Give the extent of all Plasmodium malariae-infected red blood cells.
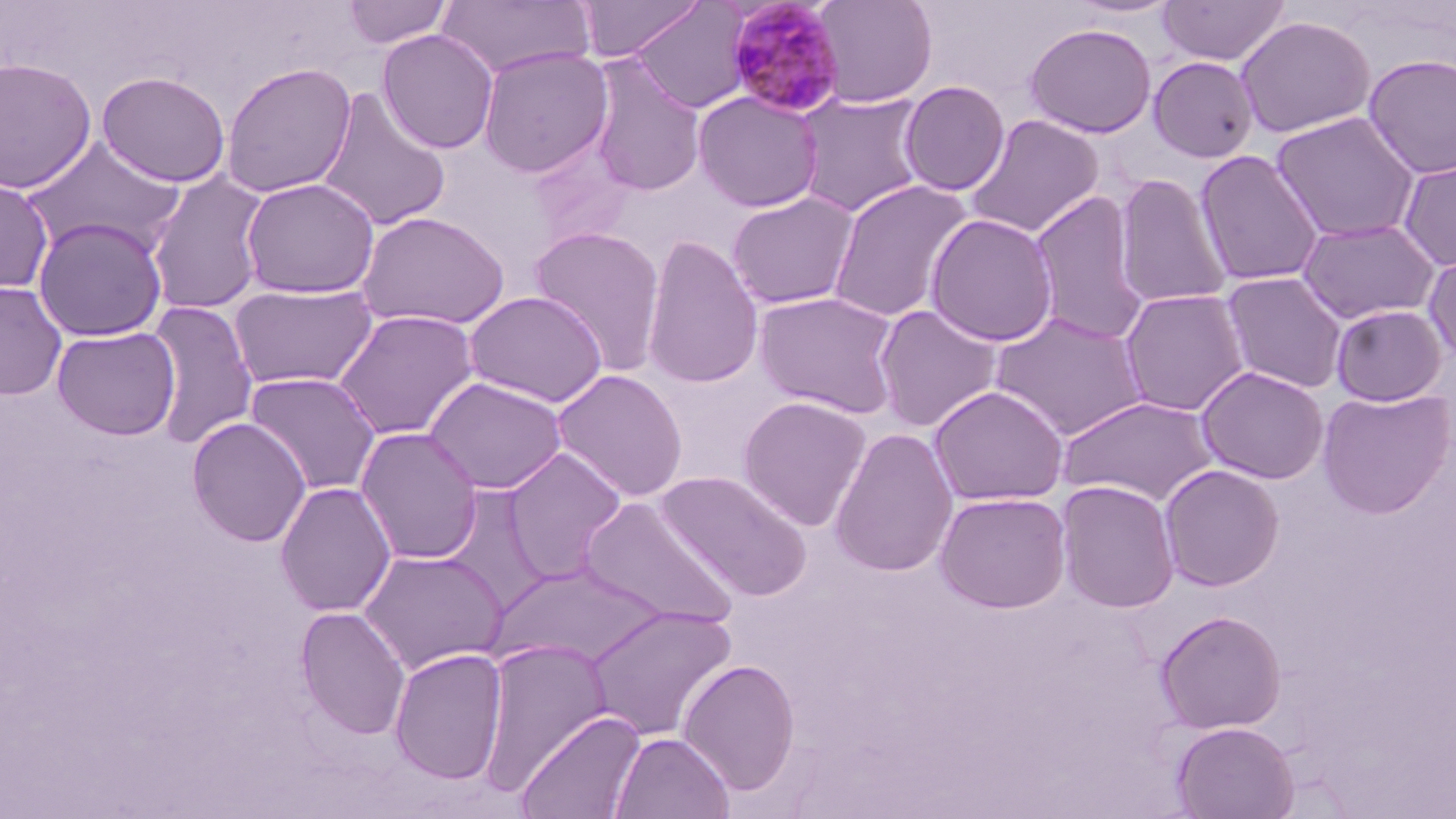

Approximate bounding boxes as (x1,y1)-(x2,y2) corner pairs in pixels.
Plasmodium malariae-infected red blood cells: (725,0)-(847,118).

slide-level diagnosis = Plasmodium malariae
field of view = one of a larger specimen
uninfected red blood cell locations = approximate bounding boxes as (x1,y1)-(x2,y2) corner pairs in pixels: (341,0)-(453,49), (573,0)-(704,62), (813,0)-(938,107), (1064,0)-(1182,19), (1156,0)-(1290,67), (434,1)-(594,80), (628,1)-(753,113), (1235,15)-(1375,138), (1024,22)-(1158,138), (377,29)-(499,154), (477,46)-(614,179), (1362,54)-(1456,179), (586,56)-(706,198), (1148,56)-(1259,163), (0,57)-(98,194), (221,62)-(357,198), (96,71)-(231,188), (899,80)-(1010,196), (316,89)-(451,232), (693,91)-(824,213), (795,92)-(927,217), (1270,111)-(1420,243), (964,113)-(1104,239), (21,137)-(185,258), (528,138)-(638,248), (1194,150)-(1325,287), (1397,155)-(1456,272), (146,171)-(271,316), (1113,173)-(1232,309), (1,175)-(53,293), (240,178)-(380,300), (827,179)-(973,323), (1029,190)-(1152,345), (726,191)-(860,310), (355,210)-(510,331), (925,213)-(1058,347), (33,217)-(168,342), (1297,217)-(1441,325), (528,225)-(666,375), (641,234)-(764,391), (1423,250)-(1456,367), (1220,271)-(1349,394), (0,281)-(67,401), (229,283)-(378,391), (1119,288)-(1250,417), (464,291)-(607,408), (753,291)-(902,418), (146,299)-(258,450), (873,304)-(1003,433), (1330,304)-(1448,406), (333,309)-(479,441), (990,312)-(1150,441), (52,326)-(180,441), (1196,365)-(1329,485), (551,368)-(688,502), (244,371)-(381,496), (425,376)-(567,495), (928,385)-(1069,506), (1316,387)-(1455,518), (737,395)-(871,531), (1058,395)-(1219,507), (186,417)-(311,548), (355,427)-(484,565), (829,427)-(959,577), (501,447)-(627,584), (1158,463)-(1285,591), (655,470)-(812,600), (1055,480)-(1179,613), (275,482)-(396,617), (435,485)-(554,614), (934,491)-(1072,613), (579,496)-(739,629), (358,549)-(508,675), (488,563)-(669,669), (584,605)-(738,742), (295,606)-(411,741), (1154,609)-(1286,734), (478,636)-(612,795), (389,648)-(508,785), (677,658)-(802,795), (514,709)-(646,819), (1170,721)-(1299,819), (611,731)-(735,818)
stain = May-Grünwald-Giemsa
preparation = thin blood smear
image size = 1456×819 pixels
magnification = 1000x
modality = optical microscopy